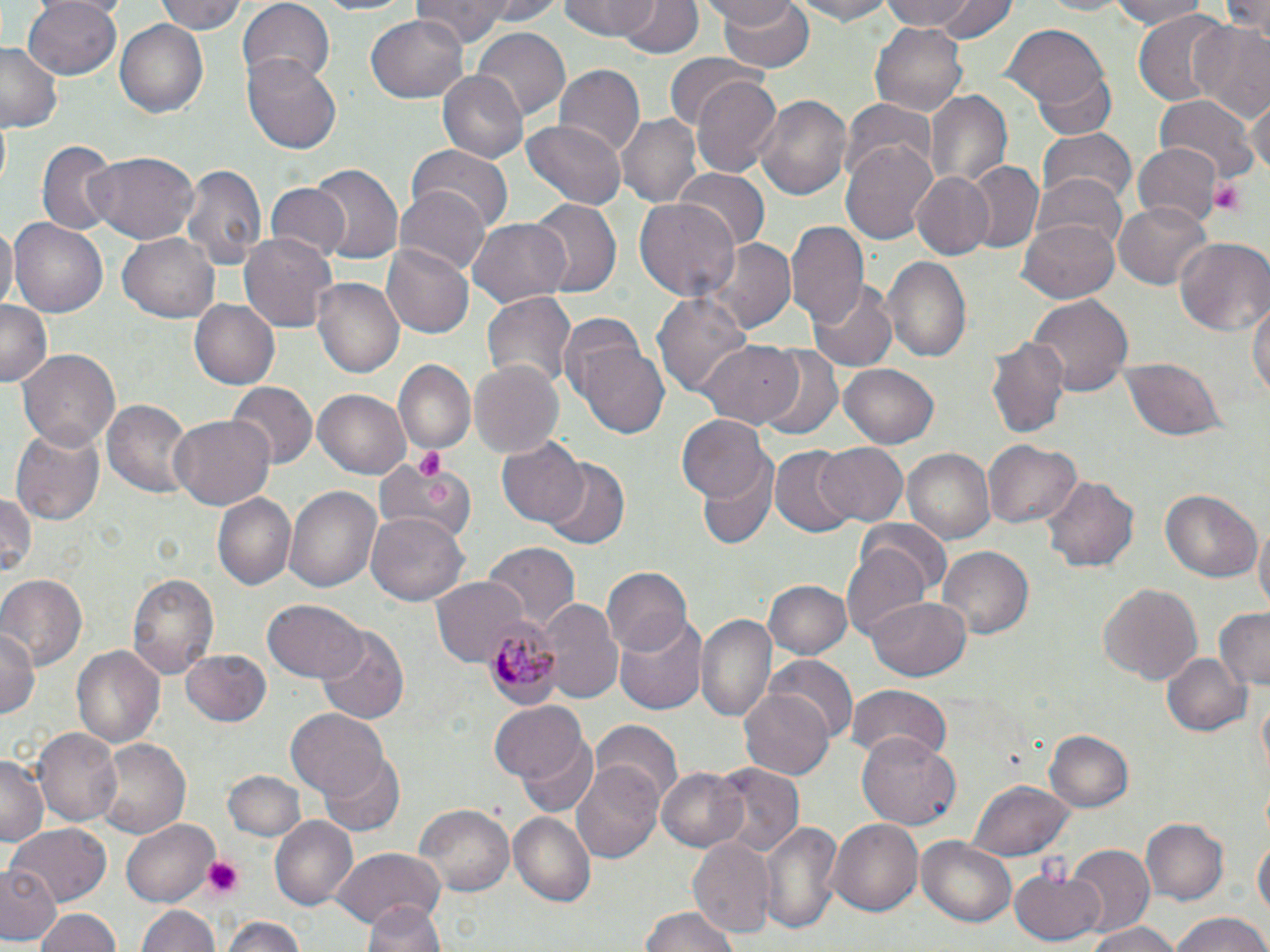

Summary:
  - Coordinate format: approximate bounding boxes as named x1/y1/x2/y2 corners in pixels
  - Platelet locations: (x1=1210, y1=177, x2=1247, y2=215), (x1=412, y1=447, x2=449, y2=480), (x1=202, y1=856, x2=244, y2=900)
  - Uninfected red blood cell locations: (x1=22, y1=0, x2=122, y2=80), (x1=153, y1=0, x2=246, y2=35), (x1=235, y1=0, x2=335, y2=86), (x1=309, y1=0, x2=427, y2=19), (x1=616, y1=0, x2=700, y2=59), (x1=706, y1=0, x2=802, y2=32), (x1=716, y1=0, x2=816, y2=73), (x1=787, y1=0, x2=899, y2=24), (x1=881, y1=0, x2=987, y2=34), (x1=930, y1=0, x2=1021, y2=45), (x1=1031, y1=0, x2=1139, y2=16), (x1=1102, y1=0, x2=1212, y2=28), (x1=1225, y1=0, x2=1269, y2=40), (x1=559, y1=1, x2=666, y2=42), (x1=410, y1=2, x2=511, y2=46), (x1=1133, y1=10, x2=1233, y2=110), (x1=366, y1=14, x2=469, y2=103), (x1=870, y1=18, x2=969, y2=116), (x1=115, y1=20, x2=209, y2=118), (x1=1190, y1=20, x2=1270, y2=122), (x1=1004, y1=25, x2=1108, y2=110), (x1=472, y1=27, x2=570, y2=118), (x1=0, y1=44, x2=65, y2=133), (x1=241, y1=53, x2=342, y2=155), (x1=663, y1=53, x2=757, y2=131), (x1=1031, y1=65, x2=1115, y2=140), (x1=556, y1=66, x2=643, y2=157), (x1=439, y1=71, x2=527, y2=162), (x1=689, y1=75, x2=783, y2=177), (x1=925, y1=90, x2=1010, y2=192), (x1=755, y1=92, x2=851, y2=202), (x1=1155, y1=95, x2=1258, y2=180), (x1=1247, y1=95, x2=1269, y2=180), (x1=840, y1=99, x2=939, y2=179), (x1=616, y1=111, x2=702, y2=206), (x1=521, y1=118, x2=629, y2=209), (x1=1036, y1=131, x2=1136, y2=208), (x1=841, y1=140, x2=939, y2=243), (x1=38, y1=141, x2=116, y2=236), (x1=408, y1=143, x2=513, y2=232), (x1=1134, y1=146, x2=1220, y2=227), (x1=87, y1=152, x2=197, y2=242), (x1=964, y1=162, x2=1044, y2=253), (x1=308, y1=163, x2=403, y2=269), (x1=180, y1=164, x2=266, y2=272), (x1=675, y1=169, x2=768, y2=248), (x1=913, y1=172, x2=996, y2=260), (x1=1032, y1=175, x2=1128, y2=258), (x1=263, y1=182, x2=350, y2=264), (x1=394, y1=186, x2=491, y2=278), (x1=635, y1=197, x2=740, y2=304), (x1=530, y1=198, x2=620, y2=300), (x1=1113, y1=202, x2=1211, y2=289), (x1=1022, y1=215, x2=1120, y2=302), (x1=8, y1=218, x2=109, y2=320), (x1=467, y1=219, x2=572, y2=308), (x1=787, y1=219, x2=867, y2=328), (x1=0, y1=222, x2=17, y2=313), (x1=238, y1=231, x2=338, y2=334), (x1=119, y1=232, x2=220, y2=322), (x1=1174, y1=235, x2=1270, y2=336), (x1=708, y1=239, x2=796, y2=334), (x1=382, y1=242, x2=475, y2=340), (x1=882, y1=256, x2=973, y2=364), (x1=311, y1=276, x2=404, y2=381), (x1=807, y1=280, x2=898, y2=371), (x1=654, y1=290, x2=753, y2=400), (x1=1250, y1=290, x2=1269, y2=407), (x1=480, y1=291, x2=576, y2=389), (x1=1029, y1=295, x2=1132, y2=397), (x1=189, y1=298, x2=279, y2=389), (x1=0, y1=300, x2=50, y2=390), (x1=557, y1=312, x2=645, y2=403), (x1=988, y1=337, x2=1071, y2=441), (x1=578, y1=343, x2=670, y2=439), (x1=697, y1=343, x2=803, y2=429), (x1=757, y1=347, x2=843, y2=442), (x1=18, y1=348, x2=120, y2=449), (x1=1120, y1=359, x2=1224, y2=441), (x1=469, y1=360, x2=564, y2=458), (x1=393, y1=362, x2=475, y2=456), (x1=837, y1=362, x2=940, y2=449), (x1=227, y1=383, x2=316, y2=470), (x1=314, y1=388, x2=413, y2=479), (x1=103, y1=397, x2=196, y2=500), (x1=676, y1=414, x2=770, y2=504), (x1=169, y1=415, x2=276, y2=510), (x1=10, y1=423, x2=104, y2=526), (x1=497, y1=438, x2=588, y2=528), (x1=985, y1=440, x2=1082, y2=532), (x1=814, y1=442, x2=909, y2=528), (x1=771, y1=446, x2=856, y2=535), (x1=901, y1=446, x2=996, y2=544), (x1=375, y1=456, x2=472, y2=544), (x1=540, y1=458, x2=630, y2=549), (x1=695, y1=459, x2=779, y2=551), (x1=1041, y1=475, x2=1137, y2=571), (x1=286, y1=485, x2=383, y2=594), (x1=1161, y1=489, x2=1261, y2=583), (x1=0, y1=491, x2=36, y2=581), (x1=210, y1=491, x2=295, y2=592), (x1=367, y1=512, x2=471, y2=606), (x1=1253, y1=521, x2=1270, y2=620), (x1=481, y1=542, x2=581, y2=633), (x1=841, y1=544, x2=934, y2=646), (x1=937, y1=545, x2=1034, y2=639), (x1=602, y1=567, x2=692, y2=654), (x1=129, y1=571, x2=218, y2=682), (x1=0, y1=574, x2=86, y2=668), (x1=429, y1=578, x2=527, y2=665), (x1=763, y1=580, x2=849, y2=659), (x1=1097, y1=582, x2=1203, y2=686), (x1=867, y1=596, x2=971, y2=680), (x1=263, y1=599, x2=365, y2=683), (x1=540, y1=599, x2=624, y2=703), (x1=1213, y1=607, x2=1270, y2=687), (x1=697, y1=612, x2=775, y2=720), (x1=615, y1=616, x2=707, y2=716), (x1=0, y1=626, x2=39, y2=721), (x1=315, y1=628, x2=407, y2=724), (x1=71, y1=645, x2=165, y2=751), (x1=180, y1=649, x2=273, y2=727), (x1=1160, y1=651, x2=1250, y2=738), (x1=767, y1=656, x2=855, y2=743), (x1=846, y1=685, x2=950, y2=765), (x1=739, y1=687, x2=834, y2=782), (x1=487, y1=703, x2=587, y2=786), (x1=288, y1=709, x2=388, y2=800), (x1=593, y1=718, x2=682, y2=805), (x1=33, y1=729, x2=122, y2=826), (x1=1043, y1=730, x2=1134, y2=815), (x1=858, y1=731, x2=961, y2=830), (x1=520, y1=735, x2=598, y2=817), (x1=94, y1=738, x2=191, y2=839), (x1=321, y1=754, x2=405, y2=836), (x1=573, y1=754, x2=664, y2=860), (x1=0, y1=756, x2=47, y2=844), (x1=708, y1=762, x2=805, y2=860), (x1=657, y1=766, x2=750, y2=852), (x1=221, y1=770, x2=307, y2=843), (x1=969, y1=779, x2=1074, y2=860), (x1=416, y1=804, x2=512, y2=893), (x1=508, y1=813, x2=595, y2=906), (x1=268, y1=816, x2=358, y2=910), (x1=830, y1=818, x2=923, y2=917), (x1=122, y1=820, x2=219, y2=905), (x1=760, y1=820, x2=842, y2=933), (x1=1142, y1=820, x2=1227, y2=904), (x1=6, y1=824, x2=111, y2=904), (x1=1254, y1=833, x2=1269, y2=922), (x1=918, y1=835, x2=1018, y2=927), (x1=689, y1=837, x2=775, y2=937), (x1=1062, y1=846, x2=1154, y2=939), (x1=330, y1=848, x2=444, y2=930), (x1=3, y1=863, x2=61, y2=944), (x1=1010, y1=869, x2=1105, y2=945), (x1=365, y1=899, x2=444, y2=952), (x1=138, y1=904, x2=219, y2=952), (x1=33, y1=907, x2=123, y2=952), (x1=640, y1=908, x2=736, y2=952), (x1=1166, y1=912, x2=1270, y2=952), (x1=220, y1=915, x2=308, y2=952), (x1=1083, y1=922, x2=1184, y2=952)
  - Plasmodium malariae-infected red blood cell locations: (x1=482, y1=614, x2=556, y2=707)
  - Slide-level diagnosis: Plasmodium malariae
  - Magnification: 1000x
  - Preparation: thin blood film
  - Image size: 1270×952 pixels
  - Stain: May-Grünwald-Giemsa
  - Field of view: single
  - Modality: optical microscopy